Outline each Plasmodium falciparum-infected red blood cell.
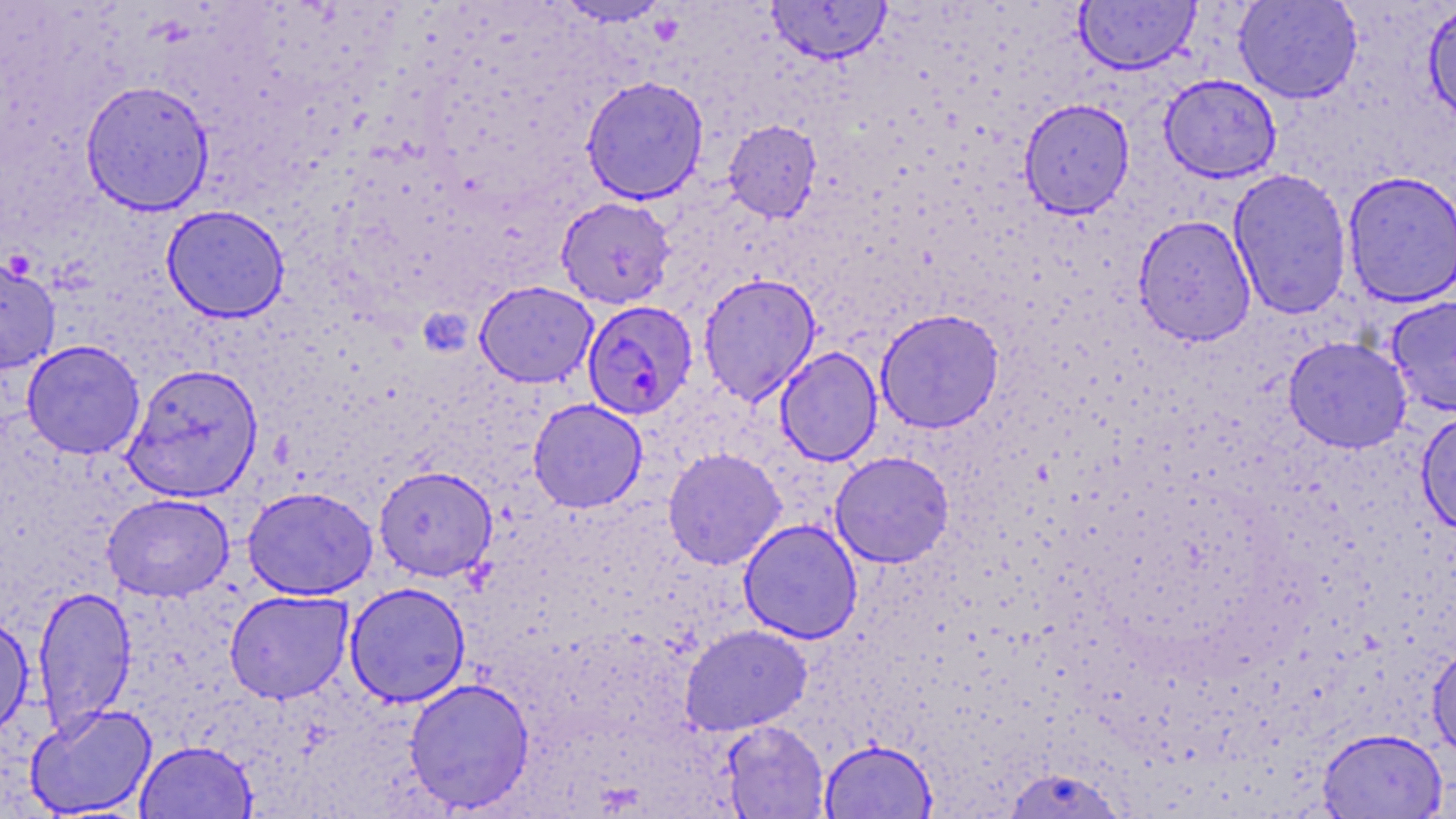

Approximate bounding boxes as (x1, y1, x2, y2) in pixels.
Plasmodium falciparum-infected red blood cells: (582, 300, 698, 420).

Summary:
  - Uninfected red blood cell locations: (550, 0, 676, 27), (1233, 0, 1363, 104), (765, 1, 892, 65), (1074, 1, 1201, 75), (1422, 2, 1456, 130), (1158, 74, 1282, 183), (581, 76, 709, 204), (79, 80, 215, 216), (1019, 98, 1135, 218), (723, 120, 821, 222), (1228, 168, 1353, 320), (1341, 170, 1456, 307), (555, 196, 676, 309), (161, 204, 290, 323), (1133, 214, 1256, 346), (0, 256, 61, 374), (698, 272, 821, 406), (474, 280, 598, 388), (1386, 296, 1456, 417), (875, 308, 1005, 433), (1283, 336, 1412, 453), (21, 340, 146, 460), (775, 346, 883, 466), (122, 363, 264, 502), (528, 398, 648, 512), (1416, 410, 1456, 535), (662, 447, 786, 570), (830, 451, 954, 568), (373, 465, 498, 581), (242, 486, 378, 600), (102, 493, 234, 601), (738, 519, 863, 644), (344, 582, 471, 707), (32, 585, 137, 737), (224, 589, 354, 704), (0, 611, 34, 741), (680, 625, 811, 735), (1427, 645, 1456, 759), (404, 677, 535, 813), (24, 703, 157, 817), (720, 720, 830, 818), (1318, 728, 1447, 819), (819, 739, 938, 819), (134, 740, 257, 819), (1002, 767, 1127, 819)
  - Slide-level diagnosis: Plasmodium falciparum
  - Preparation: thin blood film
  - Image size: 1456×819 pixels
  - Modality: optical microscopy
  - Magnification: 1000x
  - Stain: May-Grünwald-Giemsa
  - Field of view: one of a larger specimen